Describe the morphology of the red blood cells.
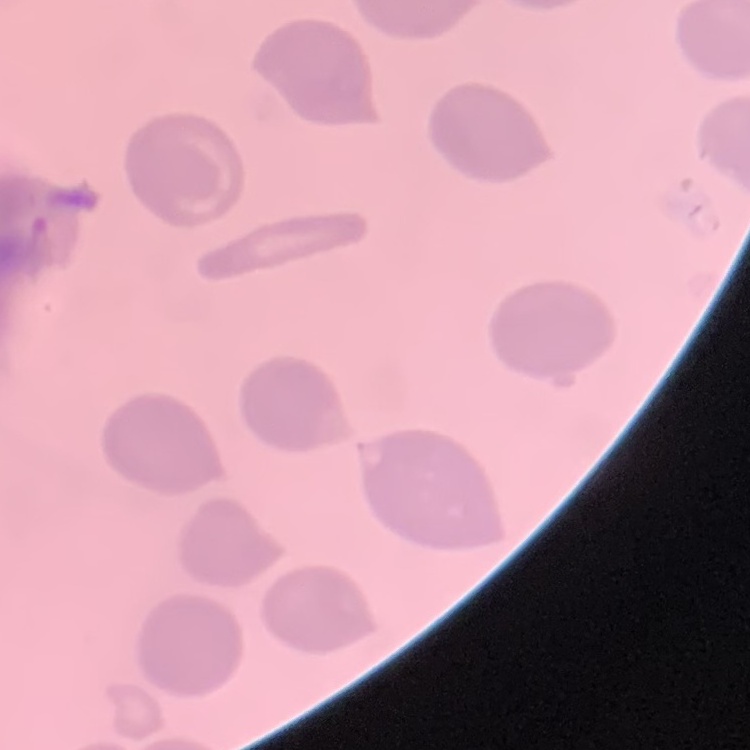

No rouleaux formation.

Thin blood smear. Stained with either Field's or Giemsa. Square crop of a larger photomicrograph.